Point out each malaria parasite and each leukocyte.
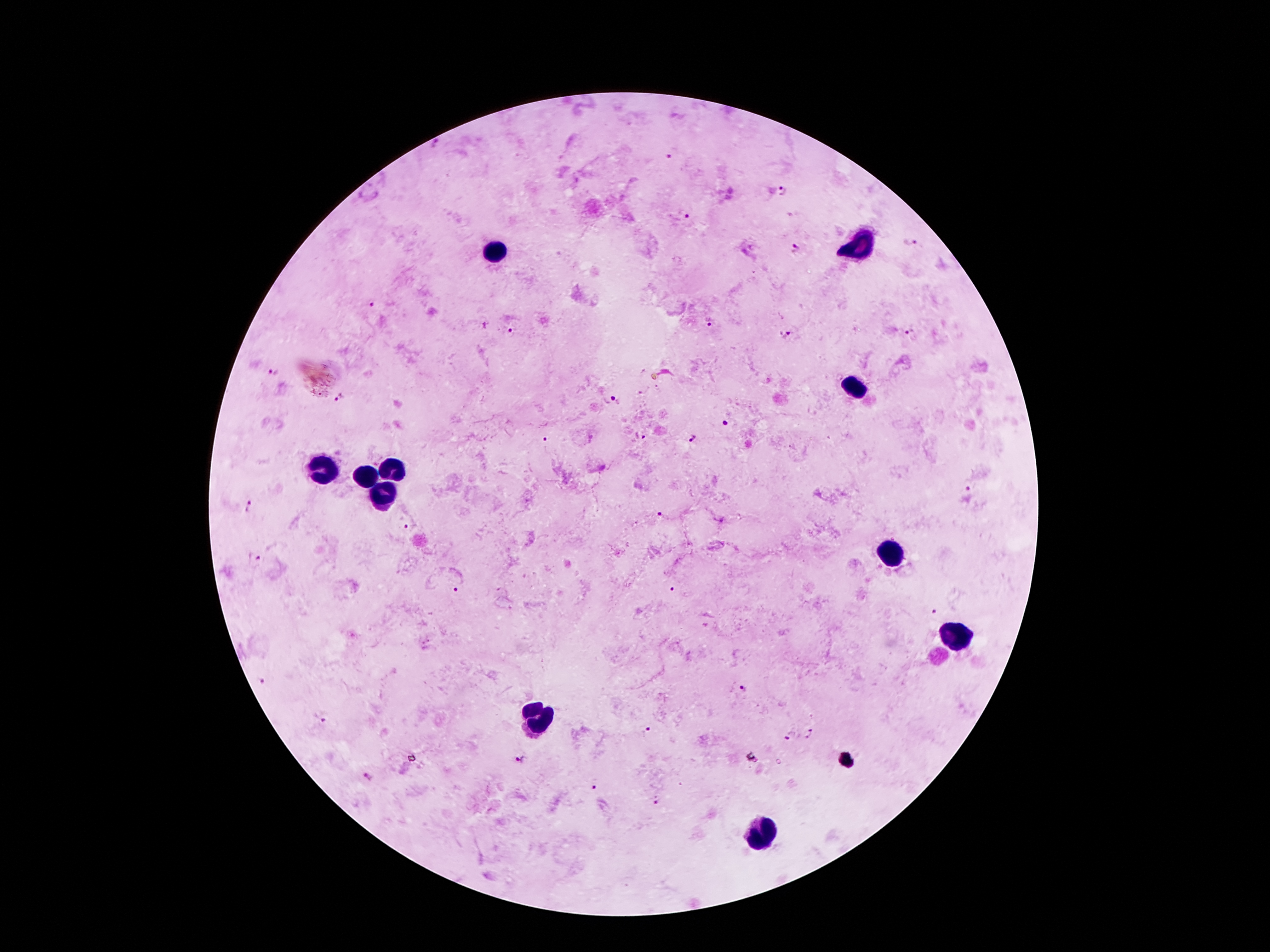

Approximate centers as {x, y} in pixels.
Malaria parasites: {672, 152}, {785, 189}, {685, 213}, {912, 243}, {795, 247}, {371, 303}, {710, 325}, {512, 328}, {911, 328}, {786, 335}, {273, 371}, {340, 398}, {615, 399}, {726, 422}, {640, 437}, {694, 438}, {544, 440}, {968, 488}, {249, 506}, {659, 516}, {410, 525}, {253, 558}, {674, 589}, {456, 592}, {936, 611}, {260, 681}, {744, 689}, {325, 716}, {647, 732}, {812, 735}, {790, 737}, {517, 760}, {367, 777}, {594, 785}, {653, 800}.
Leukocytes: {859, 246}, {496, 251}, {857, 392}, {396, 468}, {322, 470}, {367, 476}, {383, 496}, {894, 556}, {953, 632}, {541, 722}, {762, 837}.

patient_malaria_status: positive for Plasmodium falciparum
stain: Giemsa
field_of_view: one from this slide
capture: smartphone through the microscope eyepiece
image_size: 1270×952 pixels
magnification: 100x
preparation: thick peripheral-blood smear